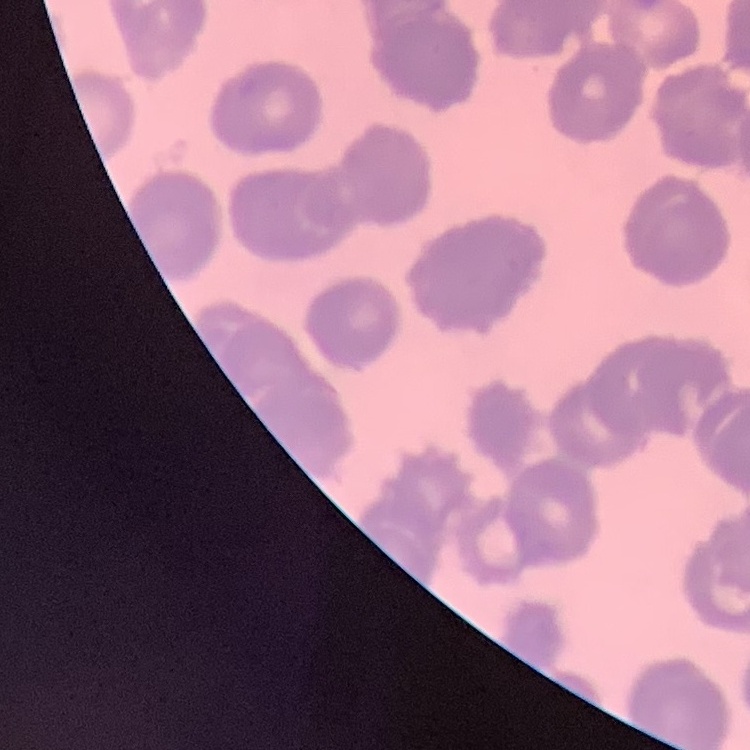 The red blood cells exhibit rouleaux formation. Square crop of a larger photomicrograph. Field's or Giemsa stain. Thin blood film.